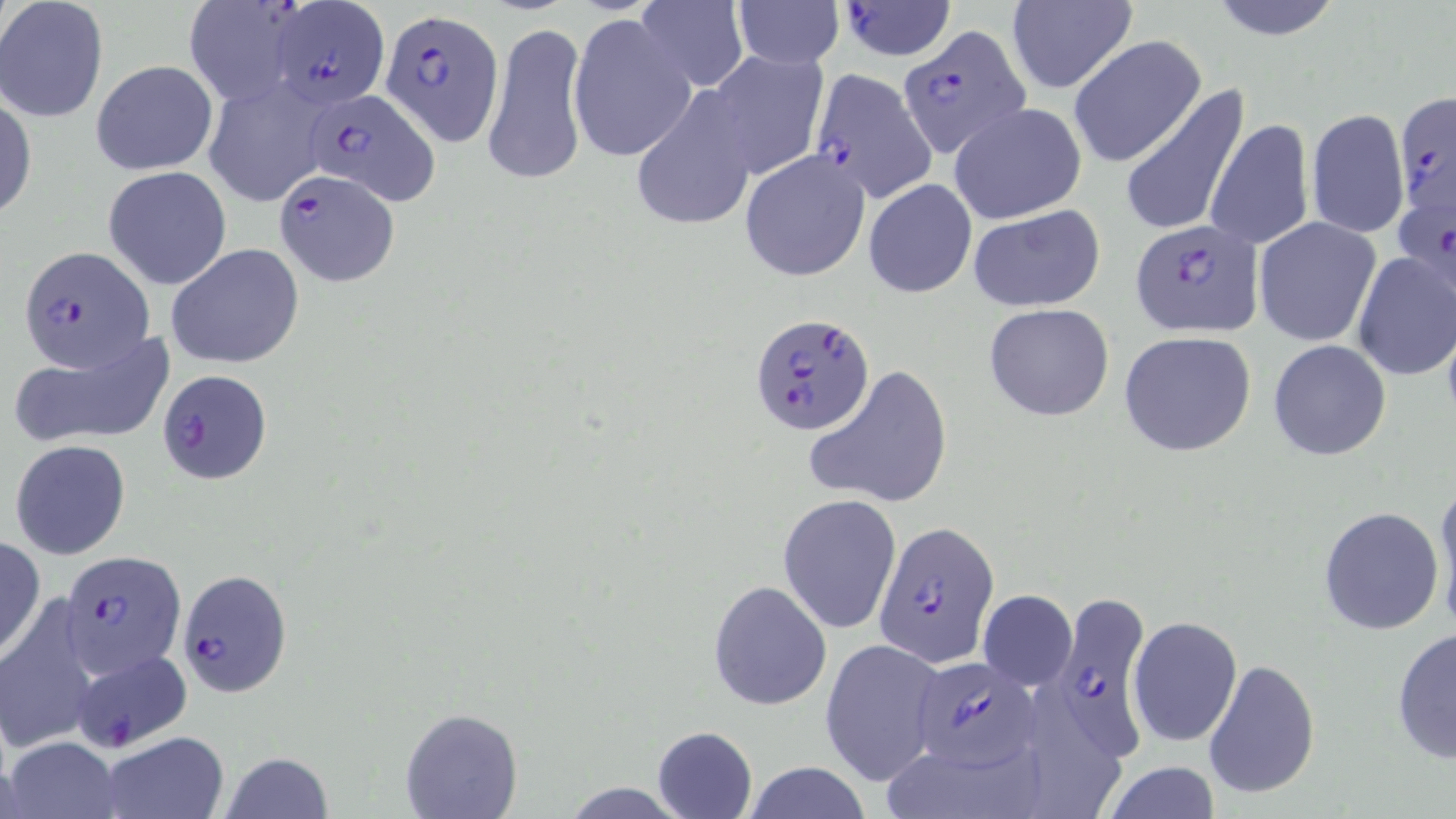
Approximate bounding boxes as named x1/y1/x2/y2 corners in pixels. Plasmodium falciparum-infected red blood cell locations: (x1=182, y1=2, x2=307, y2=105), (x1=265, y1=2, x2=389, y2=110), (x1=836, y1=2, x2=957, y2=60), (x1=380, y1=8, x2=503, y2=144), (x1=897, y1=25, x2=1030, y2=157), (x1=807, y1=69, x2=939, y2=202), (x1=304, y1=88, x2=438, y2=204), (x1=1393, y1=88, x2=1453, y2=216), (x1=274, y1=168, x2=400, y2=285), (x1=1394, y1=198, x2=1452, y2=292), (x1=1129, y1=218, x2=1264, y2=338), (x1=16, y1=245, x2=151, y2=371), (x1=749, y1=314, x2=876, y2=435), (x1=158, y1=369, x2=272, y2=482), (x1=873, y1=523, x2=998, y2=666), (x1=59, y1=550, x2=185, y2=681), (x1=178, y1=568, x2=294, y2=697), (x1=1046, y1=593, x2=1151, y2=759), (x1=68, y1=649, x2=192, y2=751), (x1=907, y1=657, x2=1039, y2=769). Uninfected red blood cell locations: (x1=1204, y1=0, x2=1347, y2=41), (x1=0, y1=1, x2=109, y2=124), (x1=633, y1=1, x2=749, y2=91), (x1=732, y1=1, x2=842, y2=71), (x1=1005, y1=1, x2=1137, y2=93), (x1=568, y1=13, x2=695, y2=161), (x1=482, y1=20, x2=590, y2=192), (x1=1067, y1=35, x2=1207, y2=167), (x1=700, y1=50, x2=829, y2=181), (x1=90, y1=59, x2=218, y2=175), (x1=202, y1=77, x2=331, y2=206), (x1=1120, y1=81, x2=1251, y2=240), (x1=632, y1=90, x2=759, y2=227), (x1=1, y1=91, x2=37, y2=222), (x1=949, y1=102, x2=1088, y2=225), (x1=1305, y1=108, x2=1409, y2=239), (x1=1206, y1=118, x2=1316, y2=251), (x1=740, y1=149, x2=870, y2=281), (x1=103, y1=166, x2=232, y2=290), (x1=863, y1=177, x2=977, y2=299), (x1=966, y1=205, x2=1107, y2=313), (x1=1254, y1=218, x2=1380, y2=346), (x1=166, y1=242, x2=305, y2=370), (x1=1351, y1=250, x2=1455, y2=381), (x1=983, y1=302, x2=1115, y2=422), (x1=8, y1=330, x2=176, y2=450), (x1=1118, y1=331, x2=1258, y2=457), (x1=1268, y1=339, x2=1392, y2=462), (x1=807, y1=364, x2=953, y2=509), (x1=10, y1=439, x2=132, y2=560), (x1=1432, y1=481, x2=1456, y2=629), (x1=778, y1=494, x2=901, y2=633), (x1=1317, y1=505, x2=1444, y2=634), (x1=0, y1=538, x2=46, y2=660), (x1=708, y1=580, x2=832, y2=711), (x1=977, y1=589, x2=1076, y2=691), (x1=1, y1=600, x2=101, y2=755), (x1=1127, y1=616, x2=1243, y2=748), (x1=1391, y1=627, x2=1455, y2=764), (x1=819, y1=638, x2=948, y2=786), (x1=1203, y1=657, x2=1322, y2=802), (x1=1023, y1=686, x2=1121, y2=818), (x1=399, y1=707, x2=524, y2=819), (x1=652, y1=726, x2=758, y2=818), (x1=99, y1=732, x2=228, y2=818), (x1=3, y1=736, x2=122, y2=818), (x1=892, y1=748, x2=1047, y2=815), (x1=220, y1=751, x2=333, y2=818), (x1=739, y1=762, x2=874, y2=818), (x1=1101, y1=762, x2=1222, y2=818). Slide-level diagnosis: Plasmodium falciparum. Light microscopy. Single field of view. Image is 1456×819 pixels. May-Grünwald-Giemsa stain. 1000x magnification. Thin blood smear.